Name the blood parasite species.
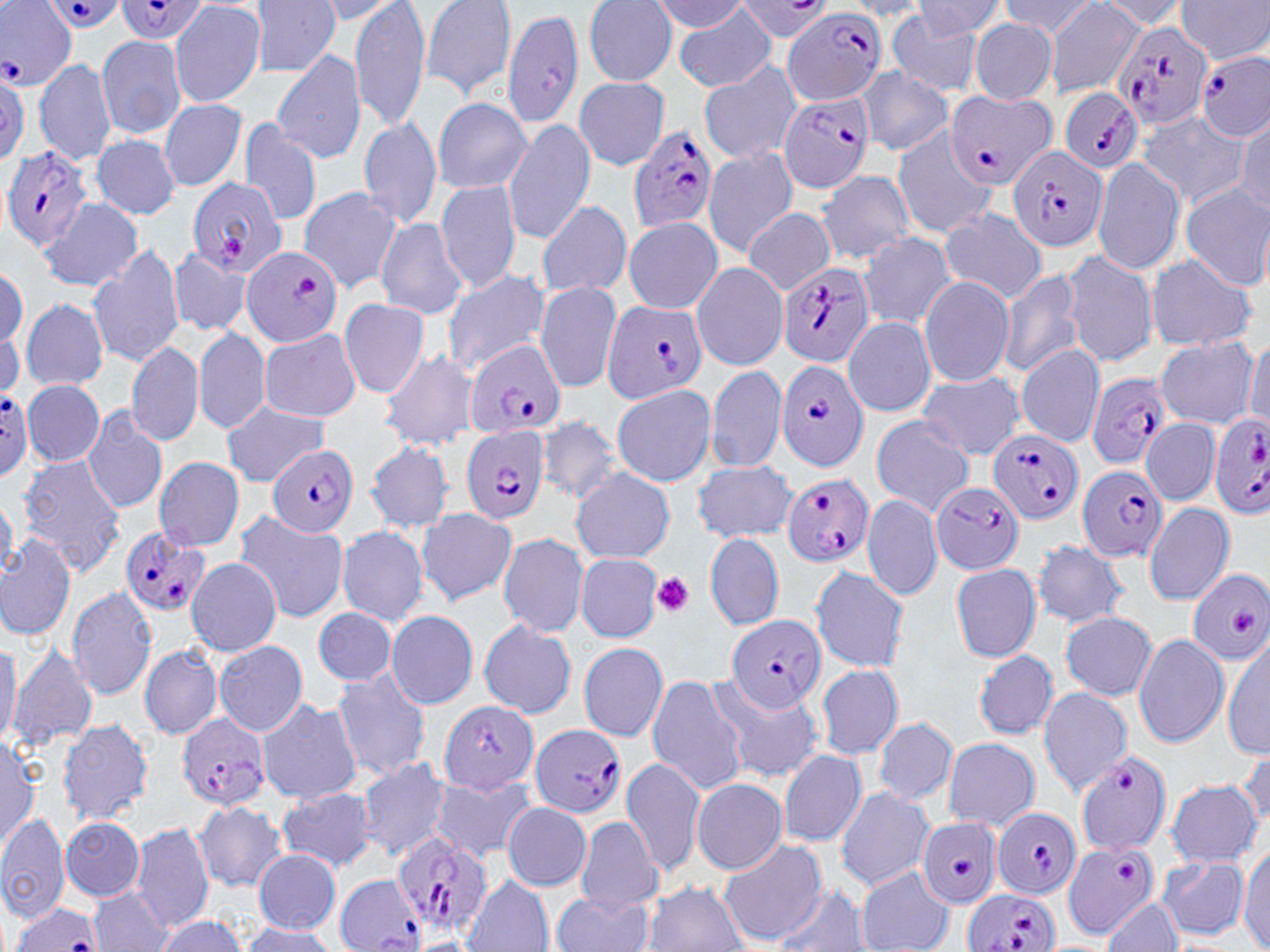
Plasmodium falciparum.

stain = May-Grünwald-Giemsa
Plasmodium falciparum-infected red blood cell locations (subset) = approximate bounding boxes as named x1/y1/x2/y2 corners in pixels: (x1=40, y1=0, x2=129, y2=33), (x1=115, y1=0, x2=213, y2=44), (x1=0, y1=1, x2=75, y2=88), (x1=732, y1=1, x2=835, y2=40), (x1=782, y1=6, x2=886, y2=107), (x1=1112, y1=18, x2=1213, y2=128), (x1=1197, y1=52, x2=1269, y2=141), (x1=944, y1=90, x2=1055, y2=189), (x1=1058, y1=90, x2=1143, y2=175), (x1=777, y1=92, x2=874, y2=194), (x1=628, y1=124, x2=719, y2=233), (x1=1007, y1=144, x2=1109, y2=251), (x1=2, y1=147, x2=91, y2=250), (x1=188, y1=177, x2=285, y2=276), (x1=242, y1=245, x2=343, y2=348), (x1=774, y1=259, x2=876, y2=368), (x1=601, y1=300, x2=708, y2=401), (x1=467, y1=341, x2=566, y2=438), (x1=775, y1=361, x2=870, y2=472), (x1=1084, y1=373, x2=1172, y2=470), (x1=0, y1=389, x2=32, y2=480), (x1=1207, y1=415, x2=1270, y2=520), (x1=460, y1=425, x2=550, y2=525), (x1=990, y1=430, x2=1084, y2=523), (x1=267, y1=443, x2=358, y2=537), (x1=1078, y1=464, x2=1170, y2=562), (x1=781, y1=473, x2=873, y2=566), (x1=931, y1=481, x2=1024, y2=574), (x1=120, y1=528, x2=212, y2=619), (x1=1186, y1=568, x2=1270, y2=664), (x1=725, y1=615, x2=826, y2=713), (x1=178, y1=714, x2=272, y2=808), (x1=530, y1=724, x2=625, y2=817), (x1=1075, y1=751, x2=1171, y2=853), (x1=992, y1=808, x2=1084, y2=900), (x1=918, y1=818, x2=1004, y2=907), (x1=390, y1=833, x2=495, y2=938), (x1=1061, y1=843, x2=1159, y2=939), (x1=962, y1=889, x2=1058, y2=952), (x1=12, y1=900, x2=102, y2=951)
platelet locations = approximate bounding boxes as named x1/y1/x2/y2 corners in pixels: (x1=652, y1=572, x2=693, y2=616)
field of view = one of a larger specimen
modality = light microscopy
image size = 1270×952 pixels
preparation = thin blood smear
uninfected red blood cell locations (subset) = approximate bounding boxes as named x1/y1/x2/y2 corners in pixels: (x1=250, y1=0, x2=340, y2=77), (x1=350, y1=0, x2=431, y2=132), (x1=420, y1=0, x2=517, y2=99), (x1=909, y1=0, x2=1008, y2=40), (x1=997, y1=0, x2=1103, y2=40), (x1=1176, y1=0, x2=1270, y2=63), (x1=313, y1=1, x2=406, y2=24), (x1=583, y1=1, x2=678, y2=86), (x1=650, y1=1, x2=752, y2=33), (x1=1044, y1=1, x2=1147, y2=97), (x1=1090, y1=1, x2=1191, y2=30), (x1=170, y1=3, x2=265, y2=108), (x1=842, y1=3, x2=935, y2=22), (x1=674, y1=4, x2=778, y2=93), (x1=502, y1=8, x2=582, y2=128), (x1=887, y1=12, x2=984, y2=96), (x1=969, y1=19, x2=1058, y2=104), (x1=95, y1=35, x2=188, y2=140), (x1=272, y1=49, x2=367, y2=165), (x1=33, y1=57, x2=117, y2=168), (x1=698, y1=62, x2=800, y2=165), (x1=856, y1=67, x2=954, y2=154), (x1=574, y1=77, x2=670, y2=170), (x1=431, y1=97, x2=532, y2=196), (x1=158, y1=100, x2=247, y2=191), (x1=1136, y1=112, x2=1249, y2=209), (x1=358, y1=114, x2=442, y2=230), (x1=238, y1=117, x2=322, y2=224), (x1=1232, y1=118, x2=1268, y2=214), (x1=502, y1=120, x2=597, y2=245), (x1=890, y1=127, x2=996, y2=238), (x1=90, y1=134, x2=181, y2=220), (x1=702, y1=147, x2=798, y2=258), (x1=1090, y1=158, x2=1186, y2=274), (x1=815, y1=170, x2=918, y2=264), (x1=436, y1=180, x2=522, y2=295), (x1=1180, y1=183, x2=1269, y2=290), (x1=297, y1=186, x2=403, y2=294), (x1=38, y1=196, x2=141, y2=293), (x1=534, y1=201, x2=633, y2=298), (x1=743, y1=207, x2=836, y2=296), (x1=939, y1=208, x2=1049, y2=302), (x1=622, y1=216, x2=723, y2=314), (x1=376, y1=217, x2=468, y2=319), (x1=857, y1=232, x2=957, y2=329), (x1=88, y1=243, x2=187, y2=368), (x1=167, y1=248, x2=253, y2=337), (x1=1060, y1=250, x2=1156, y2=366), (x1=1145, y1=255, x2=1258, y2=352), (x1=0, y1=262, x2=27, y2=353), (x1=691, y1=263, x2=789, y2=370), (x1=997, y1=266, x2=1086, y2=378), (x1=440, y1=268, x2=550, y2=377), (x1=919, y1=276, x2=1015, y2=387), (x1=536, y1=281, x2=624, y2=394), (x1=20, y1=296, x2=110, y2=391), (x1=338, y1=298, x2=430, y2=400), (x1=844, y1=316, x2=936, y2=418), (x1=194, y1=326, x2=272, y2=435), (x1=258, y1=329, x2=361, y2=421), (x1=1244, y1=335, x2=1270, y2=430), (x1=127, y1=338, x2=205, y2=447), (x1=1152, y1=338, x2=1260, y2=427), (x1=1015, y1=344, x2=1106, y2=448), (x1=378, y1=348, x2=479, y2=452), (x1=706, y1=364, x2=787, y2=473), (x1=916, y1=373, x2=1025, y2=460), (x1=24, y1=380, x2=105, y2=467), (x1=610, y1=384, x2=716, y2=488), (x1=221, y1=400, x2=334, y2=485), (x1=82, y1=407, x2=167, y2=515), (x1=871, y1=415, x2=976, y2=517), (x1=535, y1=416, x2=626, y2=504), (x1=1141, y1=416, x2=1220, y2=508), (x1=366, y1=440, x2=456, y2=532), (x1=16, y1=455, x2=127, y2=576), (x1=152, y1=457, x2=245, y2=551), (x1=693, y1=460, x2=797, y2=542), (x1=572, y1=467, x2=675, y2=564), (x1=862, y1=492, x2=943, y2=602), (x1=0, y1=495, x2=18, y2=582), (x1=1144, y1=502, x2=1234, y2=605), (x1=416, y1=507, x2=517, y2=605), (x1=233, y1=511, x2=349, y2=623), (x1=335, y1=525, x2=430, y2=627), (x1=705, y1=531, x2=784, y2=631), (x1=0, y1=532, x2=75, y2=641), (x1=498, y1=532, x2=590, y2=638), (x1=1032, y1=538, x2=1131, y2=628), (x1=576, y1=553, x2=662, y2=641), (x1=185, y1=558, x2=283, y2=656), (x1=950, y1=562, x2=1041, y2=663), (x1=810, y1=565, x2=909, y2=674), (x1=67, y1=586, x2=157, y2=700), (x1=314, y1=608, x2=395, y2=686), (x1=385, y1=610, x2=479, y2=709), (x1=1061, y1=610, x2=1155, y2=701), (x1=479, y1=619, x2=577, y2=719), (x1=1134, y1=633, x2=1231, y2=749), (x1=0, y1=634, x2=20, y2=750), (x1=1223, y1=634, x2=1270, y2=760), (x1=213, y1=640, x2=308, y2=737), (x1=577, y1=641, x2=669, y2=743), (x1=7, y1=644, x2=98, y2=750), (x1=138, y1=644, x2=222, y2=739), (x1=973, y1=649, x2=1058, y2=739), (x1=815, y1=664, x2=904, y2=759), (x1=331, y1=670, x2=431, y2=782), (x1=646, y1=675, x2=747, y2=795), (x1=708, y1=676, x2=828, y2=785), (x1=625, y1=685, x2=726, y2=865), (x1=1037, y1=686, x2=1133, y2=795), (x1=258, y1=697, x2=359, y2=805), (x1=440, y1=700, x2=538, y2=793), (x1=872, y1=716, x2=958, y2=807), (x1=56, y1=718, x2=154, y2=826), (x1=0, y1=734, x2=40, y2=851), (x1=941, y1=737, x2=1041, y2=832), (x1=1239, y1=745, x2=1270, y2=835), (x1=778, y1=750, x2=867, y2=847), (x1=356, y1=756, x2=451, y2=861), (x1=621, y1=759, x2=705, y2=877), (x1=428, y1=775, x2=536, y2=864), (x1=691, y1=779, x2=788, y2=873), (x1=1165, y1=779, x2=1263, y2=867), (x1=834, y1=787, x2=934, y2=890), (x1=276, y1=788, x2=379, y2=873), (x1=502, y1=801, x2=593, y2=891), (x1=193, y1=803, x2=286, y2=891), (x1=0, y1=814, x2=70, y2=923), (x1=60, y1=817, x2=146, y2=900), (x1=573, y1=817, x2=665, y2=914), (x1=131, y1=821, x2=215, y2=932), (x1=718, y1=839, x2=827, y2=946), (x1=1236, y1=846, x2=1270, y2=951), (x1=251, y1=847, x2=341, y2=934), (x1=1157, y1=857, x2=1249, y2=939), (x1=856, y1=868, x2=955, y2=952), (x1=461, y1=876, x2=554, y2=952), (x1=642, y1=881, x2=748, y2=952), (x1=771, y1=884, x2=869, y2=952), (x1=88, y1=886, x2=176, y2=951), (x1=553, y1=892, x2=653, y2=952), (x1=1102, y1=896, x2=1184, y2=952), (x1=152, y1=916, x2=247, y2=952), (x1=236, y1=922, x2=341, y2=950), (x1=410, y1=937, x2=479, y2=952)
magnification = 1000x